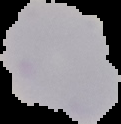

Summary:
  - Preparation: thin blood smear
  - Image type: cell region segmented out of the field of view; surrounding area masked to black
  - Image size: 121×124 pixels
  - Malaria status: uninfected